Give the preparation type.
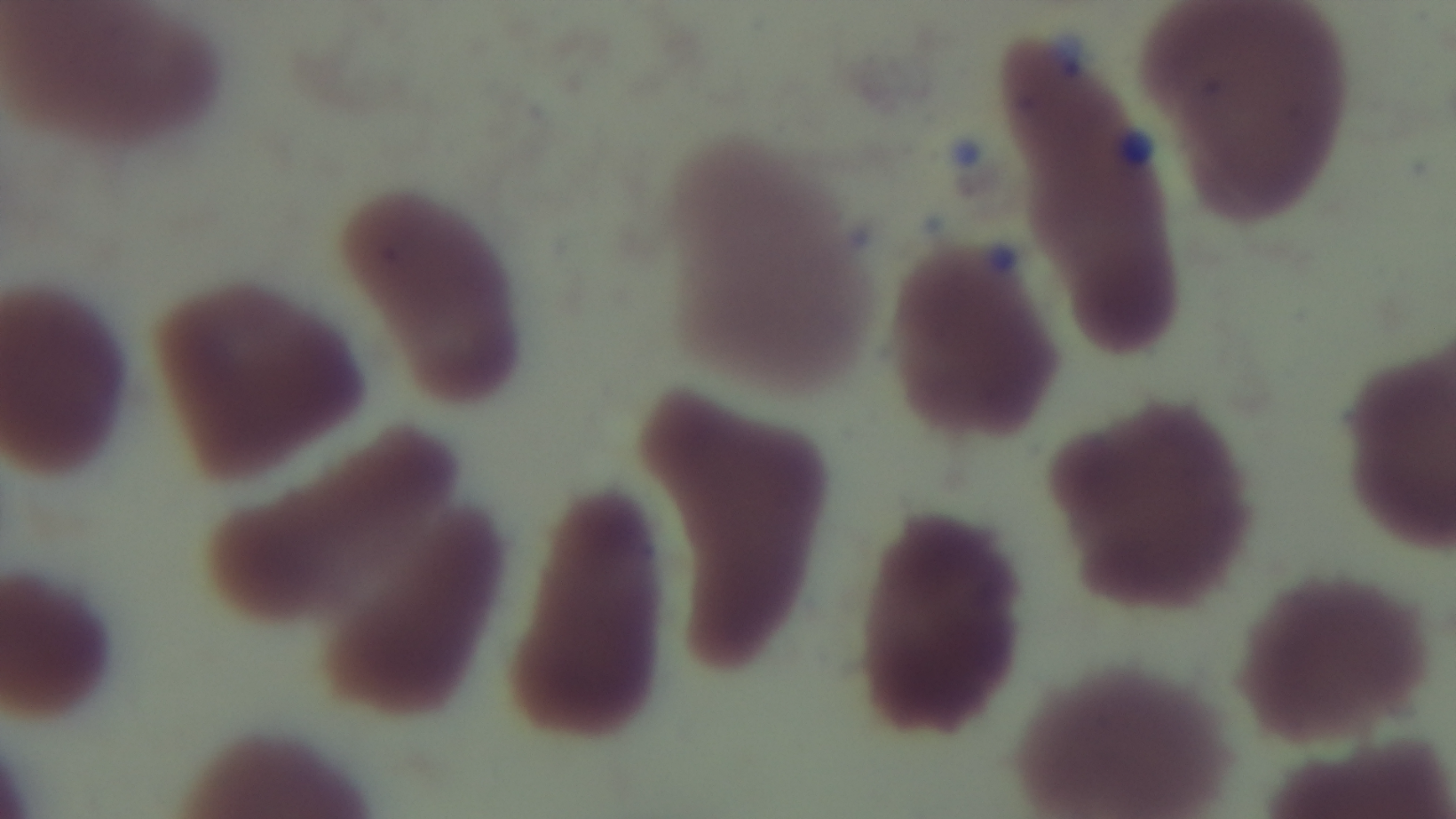
A thin smear.

Summary:
  - Field of view: single
  - Stain: Giemsa
  - Capture: mounted 4K digital camera
  - Modality: light microscopy
  - Malaria status: negative
  - Objective: 100x oil immersion